Give the position of every Plasmodium falciparum parasite, noting its life-cycle stage.
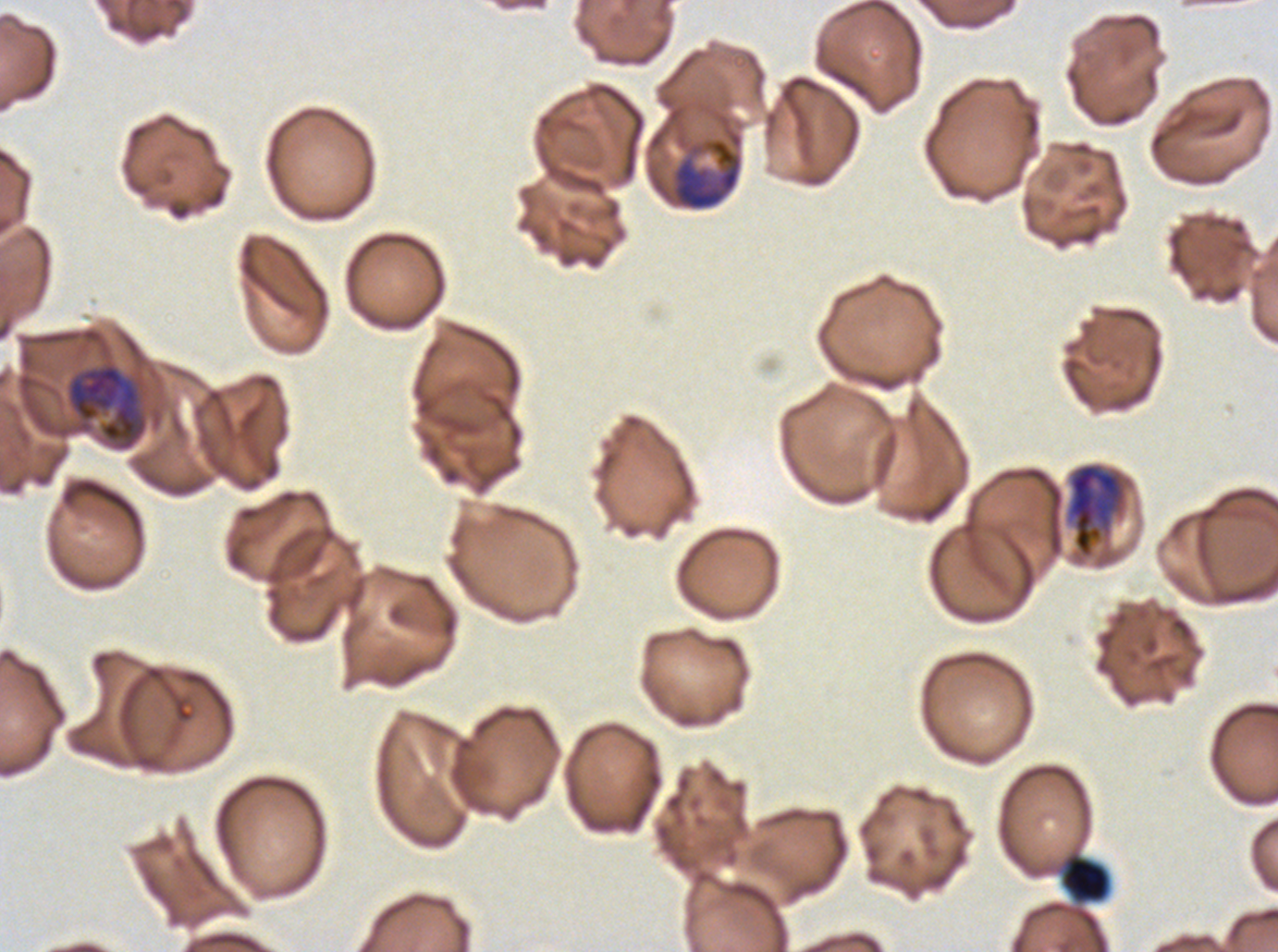

Approximate bounding rectangles given as corner coordinates in pixels from the top-left.
Early schizonts: (x1=670, y1=128, x2=743, y2=211), (x1=65, y1=360, x2=149, y2=452), (x1=1064, y1=461, x2=1128, y2=559).
No rings, late-ring/early-trophozoite forms, mid trophozoites, late trophozoites, late schizonts, segmenters, or gametocytes observed.

Debris locations: (x1=1060, y1=852, x2=1111, y2=904). One sub-image of a larger composite. Thin blood smear. Image is 1278×952 pixels. Ex-vivo Plasmodium falciparum culture from a patient in The Gambia, grown for 24 to 48 hours. Giemsa-stained preparation.